Locate platelets.
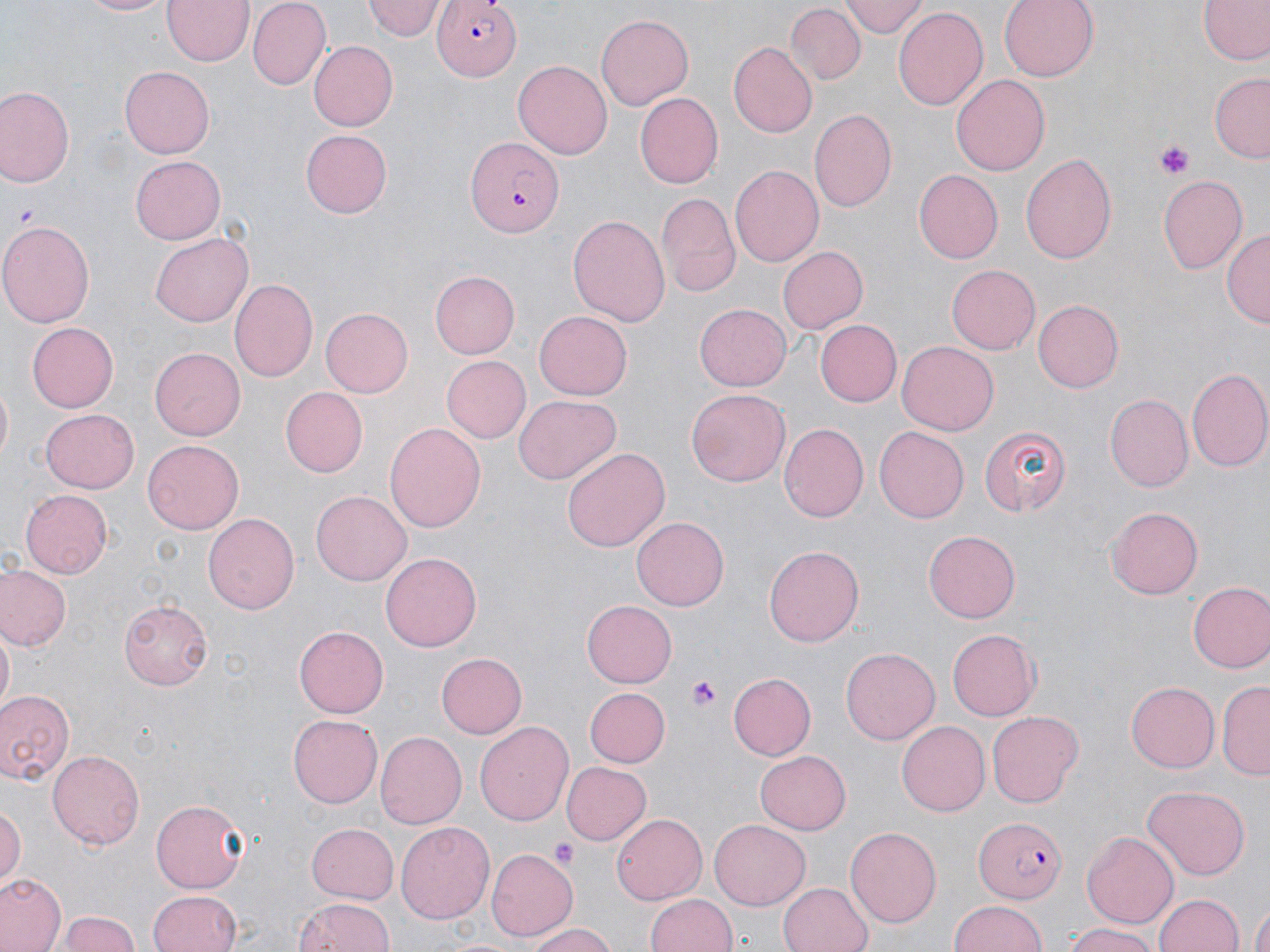
Approximate bounding boxes as (x1, y1, x2, y2) in pixels.
Platelets: (1156, 144, 1194, 177), (687, 677, 721, 711), (551, 838, 580, 869).

Summary:
  - Plasmodium falciparum-infected red blood cell locations: (433, 0, 520, 79), (465, 137, 565, 237), (974, 814, 1067, 905)
  - Uninfected red blood cell locations: (72, 0, 175, 17), (163, 0, 252, 66), (248, 0, 332, 89), (844, 0, 926, 37), (997, 0, 1099, 82), (1196, 0, 1270, 68), (362, 1, 445, 42), (788, 6, 863, 84), (895, 7, 988, 112), (596, 15, 694, 109), (308, 40, 398, 131), (727, 42, 816, 139), (514, 58, 611, 156), (120, 64, 213, 156), (1211, 72, 1270, 162), (951, 75, 1051, 176), (1, 85, 76, 189), (633, 92, 722, 189), (807, 108, 896, 211), (300, 131, 392, 217), (1021, 151, 1118, 264), (130, 155, 226, 245), (730, 165, 823, 268), (913, 171, 1002, 264), (1157, 175, 1248, 273), (657, 192, 738, 298), (568, 213, 670, 326), (0, 219, 95, 330), (1223, 229, 1269, 331), (151, 232, 252, 326), (775, 246, 867, 338), (946, 264, 1039, 354), (429, 270, 520, 358), (231, 278, 318, 383), (1033, 301, 1123, 393), (695, 304, 791, 392), (321, 309, 413, 397), (534, 309, 632, 400), (816, 321, 902, 405), (25, 322, 117, 411), (897, 340, 998, 435), (149, 347, 245, 440), (440, 356, 529, 442), (1186, 367, 1270, 474), (279, 387, 367, 477), (687, 389, 788, 489), (1105, 394, 1192, 491), (513, 395, 619, 485), (41, 410, 138, 493), (384, 420, 485, 531), (778, 425, 868, 522), (873, 425, 968, 524), (980, 425, 1069, 516), (142, 440, 243, 533), (562, 447, 669, 554), (22, 489, 113, 579), (312, 491, 411, 586), (1106, 506, 1200, 599), (203, 514, 300, 615), (633, 516, 729, 611), (924, 531, 1021, 622), (764, 544, 864, 646), (381, 553, 483, 652), (1, 567, 69, 650), (1186, 582, 1270, 674), (120, 598, 212, 689), (581, 600, 676, 686), (2, 626, 15, 709), (295, 627, 388, 717), (946, 627, 1039, 721), (840, 647, 940, 744), (436, 652, 526, 739), (726, 673, 814, 760), (1125, 681, 1220, 772), (1218, 681, 1270, 778), (583, 685, 669, 766), (0, 688, 79, 786), (987, 710, 1084, 807), (288, 714, 384, 807), (474, 720, 573, 825), (896, 721, 990, 817), (373, 732, 466, 829), (49, 749, 148, 849), (755, 749, 852, 834), (561, 761, 651, 845), (1143, 785, 1251, 879), (151, 801, 250, 892), (0, 807, 26, 884), (612, 812, 706, 904), (707, 820, 811, 910), (306, 822, 399, 905), (396, 822, 495, 924), (846, 826, 941, 928), (1082, 830, 1181, 928), (487, 848, 578, 940), (1, 874, 64, 952), (778, 881, 875, 952), (151, 891, 244, 952), (1152, 892, 1246, 952), (645, 893, 736, 952), (291, 897, 396, 952), (949, 899, 1048, 952), (1247, 903, 1270, 952), (59, 909, 143, 952), (524, 922, 619, 952), (1058, 922, 1164, 952)
  - Slide-level diagnosis: Plasmodium falciparum
  - Stain: May-Grünwald-Giemsa
  - Image size: 1270×952 pixels
  - Field of view: one of a larger specimen
  - Preparation: thin blood smear
  - Magnification: 1000x
  - Modality: optical microscopy